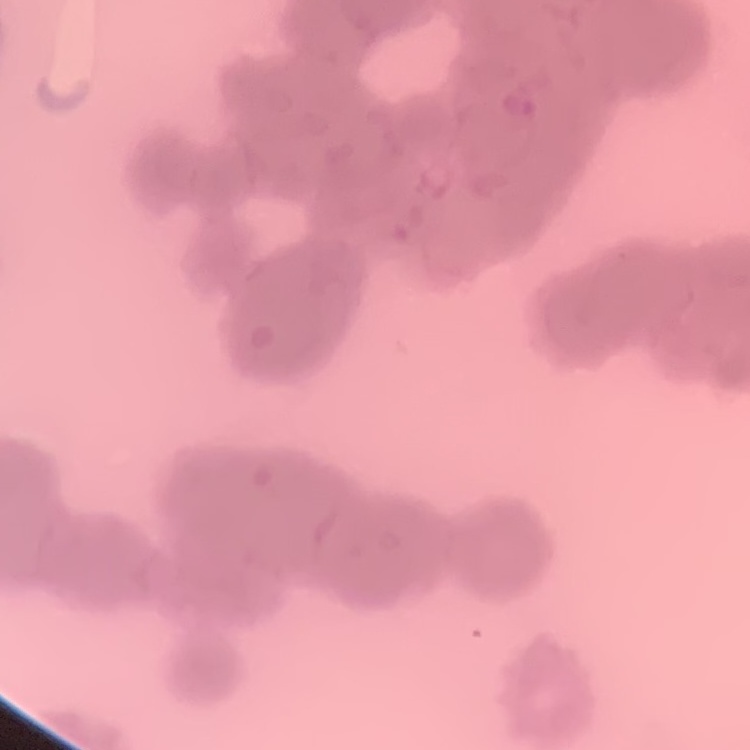
Summary:
  - Red blood cell morphology: rouleaux formation
  - Stain: Field's or Giemsa
  - Image type: square crop of a larger photomicrograph
  - Preparation: thin blood smear